Assess the morphology of the red blood cells.
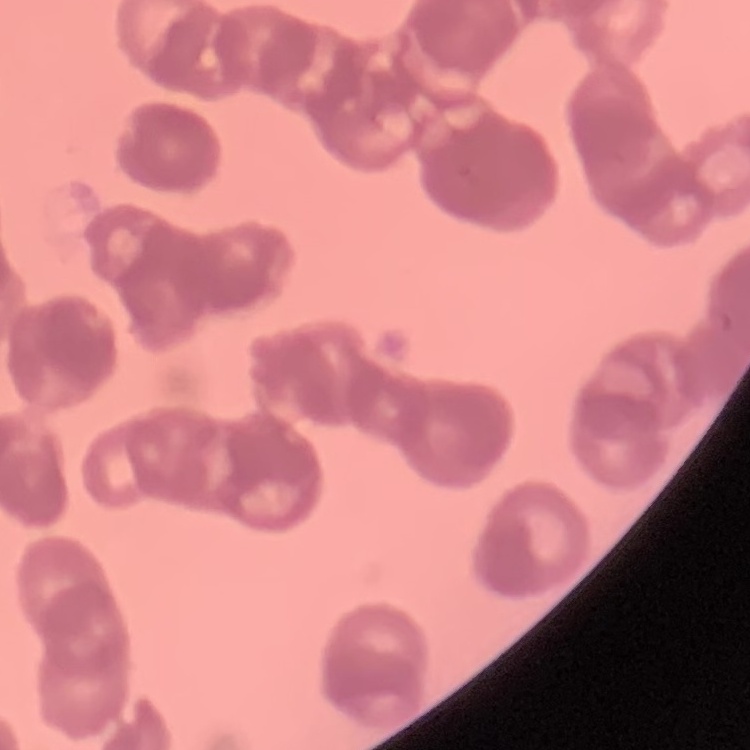

Rouleaux formation.

stain = Field's or Giemsa
image type = one tile cut from a larger photomicrograph
preparation = thin blood smear